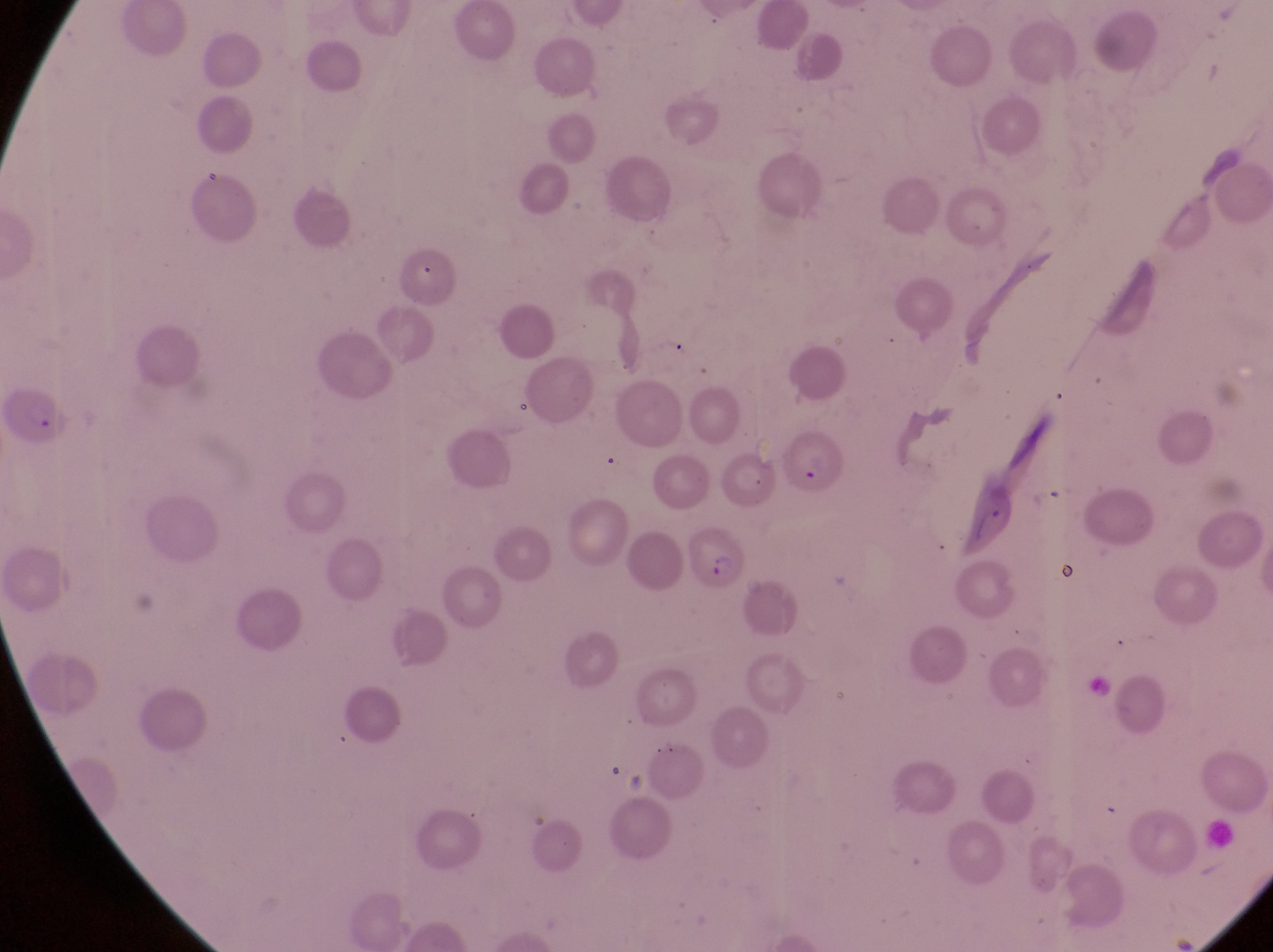
Approximate bounding boxes as [left, top, right, bottom] in pixels.
Summary:
  - Parasitised red blood cell locations: [8, 379, 73, 447], [784, 427, 847, 499], [689, 521, 742, 593]
  - Magnification: 1000x
  - Image size: 1273×952 pixels
  - Field of view: single
  - Capture: smartphone photograph through the eyepiece of an Olympus CX-23 microscope
  - Preparation: thin blood film
  - Country: Uganda